Identify the parasite.
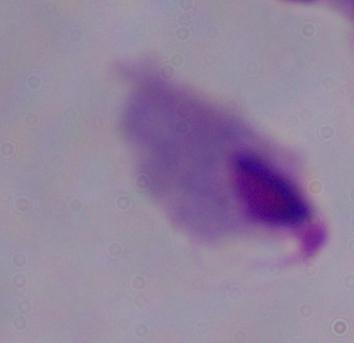
This is a trichomonad.

Summary:
  - Modality: micrograph
  - Magnification: 1000x